Report the malaria status.
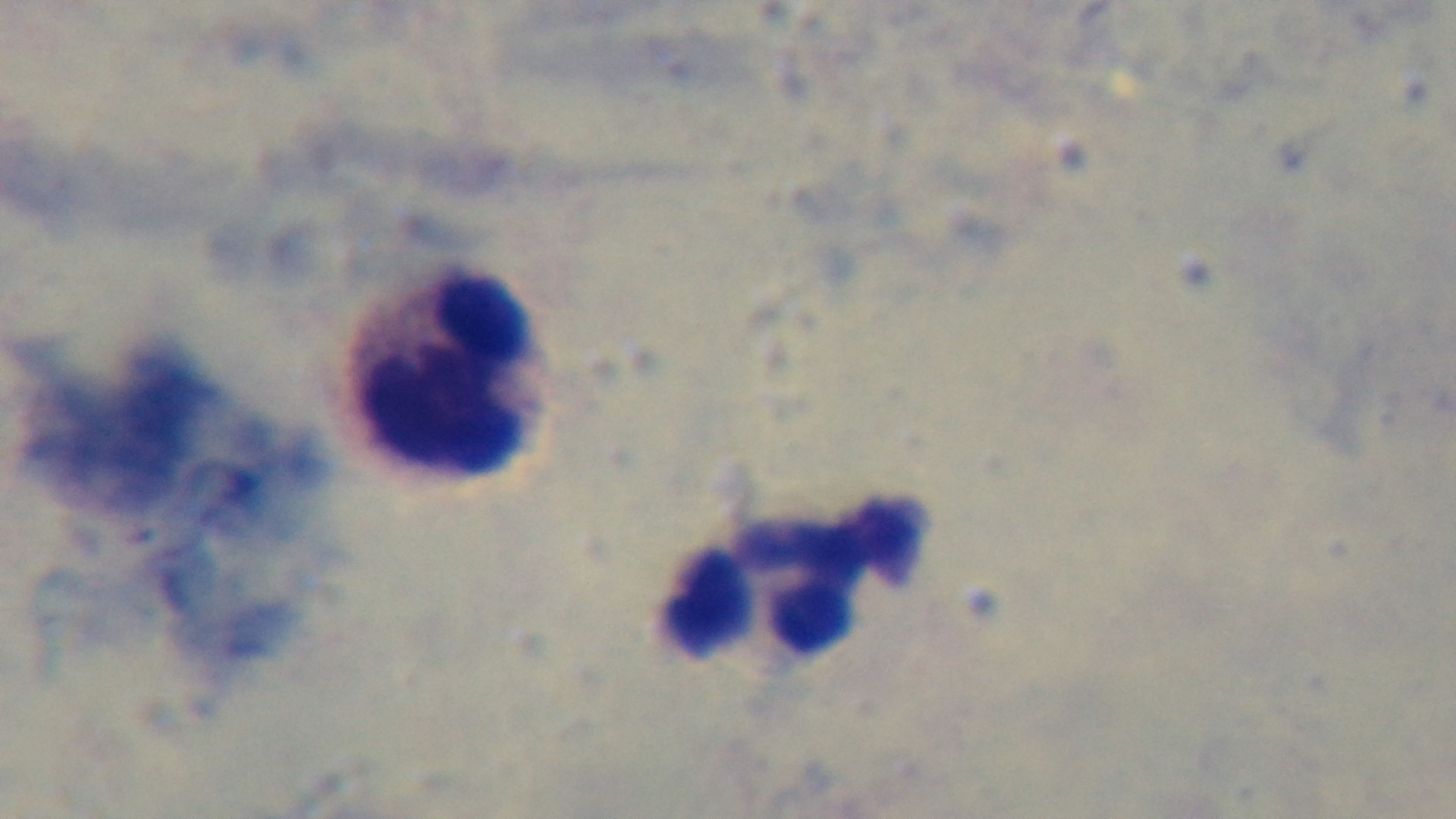

Uninfected.

Summary:
  - Modality: light microscopy
  - Field of view: single
  - Capture: mounted 4K digital camera
  - Preparation: thick
  - Objective: 100x oil immersion
  - Stain: Giemsa